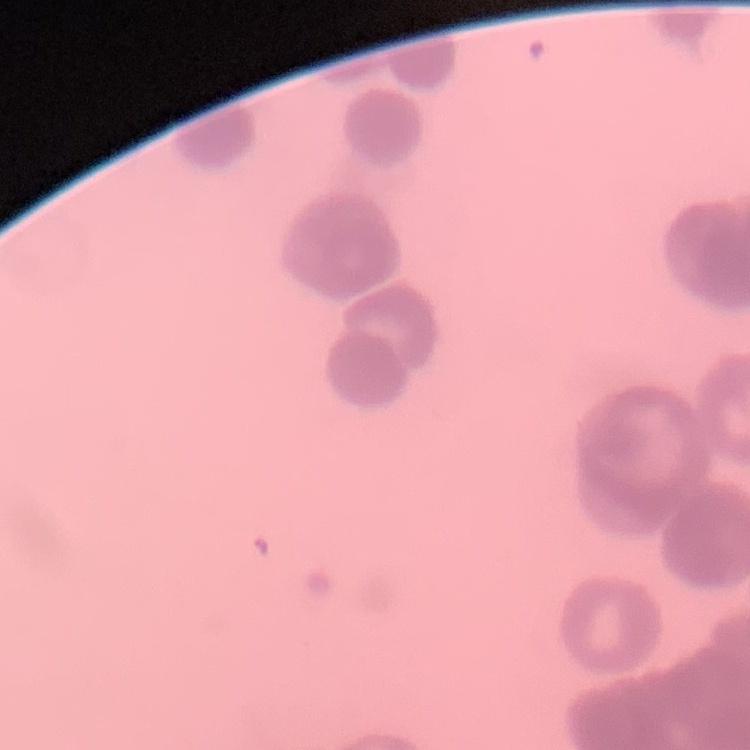

Summary:
  - Red blood cell morphology: rouleaux formation
  - Stain: Field's or Giemsa
  - Preparation: thin peripheral smear
  - Image type: square crop of a larger photomicrograph